Classify this cell by malaria status.
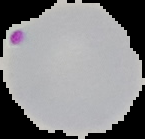
It is parasitized.

image_type: cell region segmented out of the field of view; surrounding area masked to black
image_size: 145×139 pixels
preparation: thin blood film